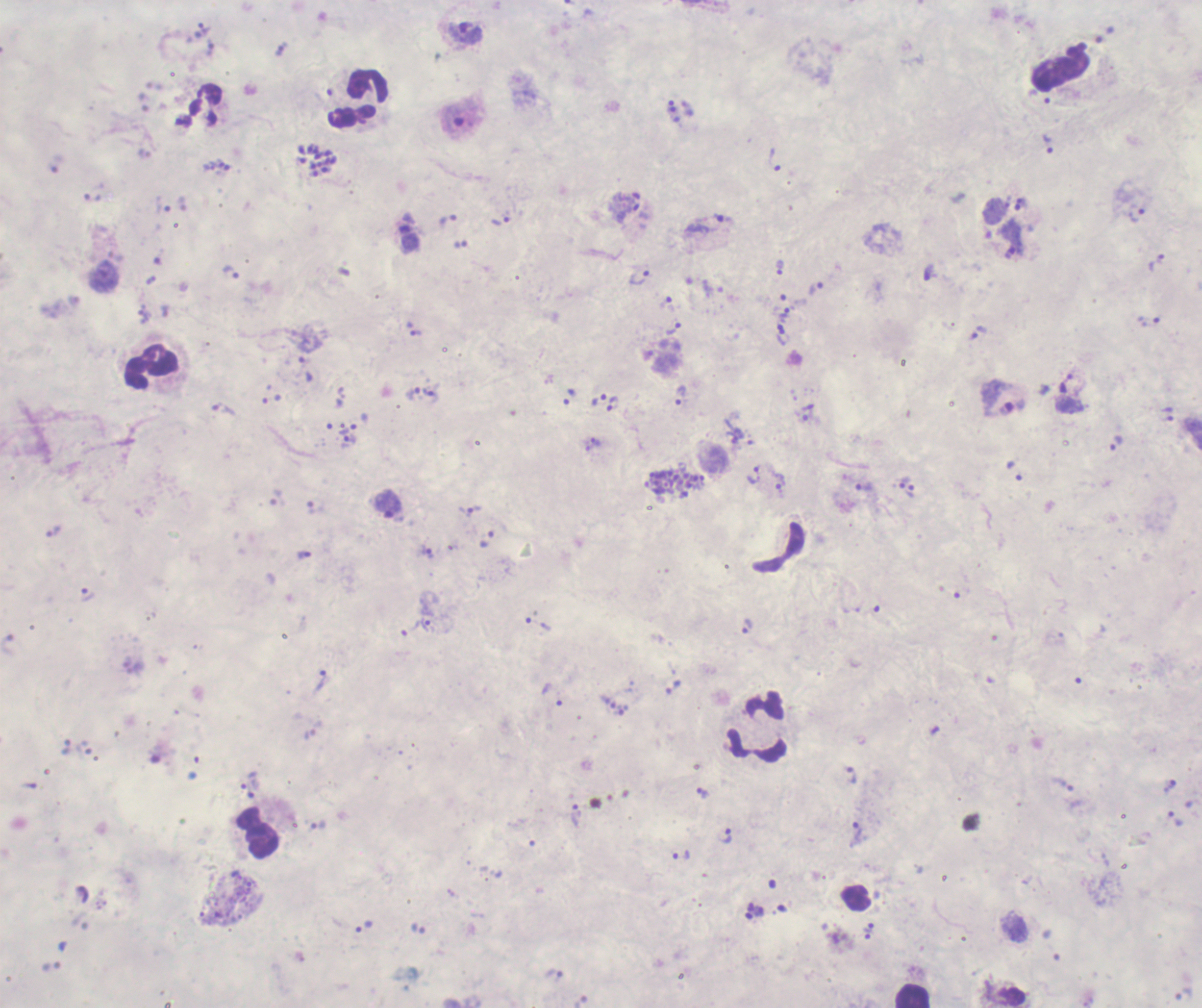

Approximate centers as {x, y} in pixels.
Summary:
  - Leukocyte locations: {357, 99}, {151, 367}, {757, 726}, {258, 832}, {913, 995}
  - Trophozoite locations: {205, 28}, {465, 33}, {281, 48}, {454, 120}, {1048, 144}, {775, 160}, {163, 204}, {628, 212}, {1137, 213}, {448, 220}, {499, 221}, {1157, 263}, {780, 267}, {231, 272}, {639, 278}, {665, 301}, {1149, 322}, {672, 329}, {416, 333}, {783, 337}, {305, 368}, {1066, 384}, {430, 392}, {412, 393}, {681, 395}, {599, 400}, {612, 404}, {224, 409}, {1169, 414}, {347, 429}, {351, 439}, {596, 441}, {1117, 443}, {754, 476}, {780, 482}, {905, 482}, {864, 486}, {910, 491}, {278, 499}, {470, 511}, {54, 532}, {428, 552}, {305, 555}, {88, 595}, {425, 624}, {748, 626}, {411, 628}, {321, 680}, {673, 687}, {623, 710}, {851, 774}, {248, 780}, {250, 790}, {702, 792}, {576, 816}, {1176, 818}, {318, 824}, {856, 831}, {725, 836}, {681, 855}, {363, 926}, {869, 928}
  - Schizont locations: {317, 160}, {676, 484}
  - Life-cycle stages observed: trophozoite, schizont
  - Preparation: thick blood smear
  - Context: previously used in an actual diagnosis
  - Image size: 1202×1008 pixels
  - Coloration quality: bad
  - Field of view: single
  - Magnification: 100x
  - Background quality: poor
  - Result: Plasmodium parasites detected
  - Stain: Romanowsky